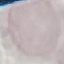
Summary:
  - Result: negative for malaria parasites
  - Capture: smartphone camera at the microscope eyepiece
  - Stain: Giemsa
  - Image type: automatically extracted cell patch, resized to 64 × 64 pixels
  - Preparation: thin smear